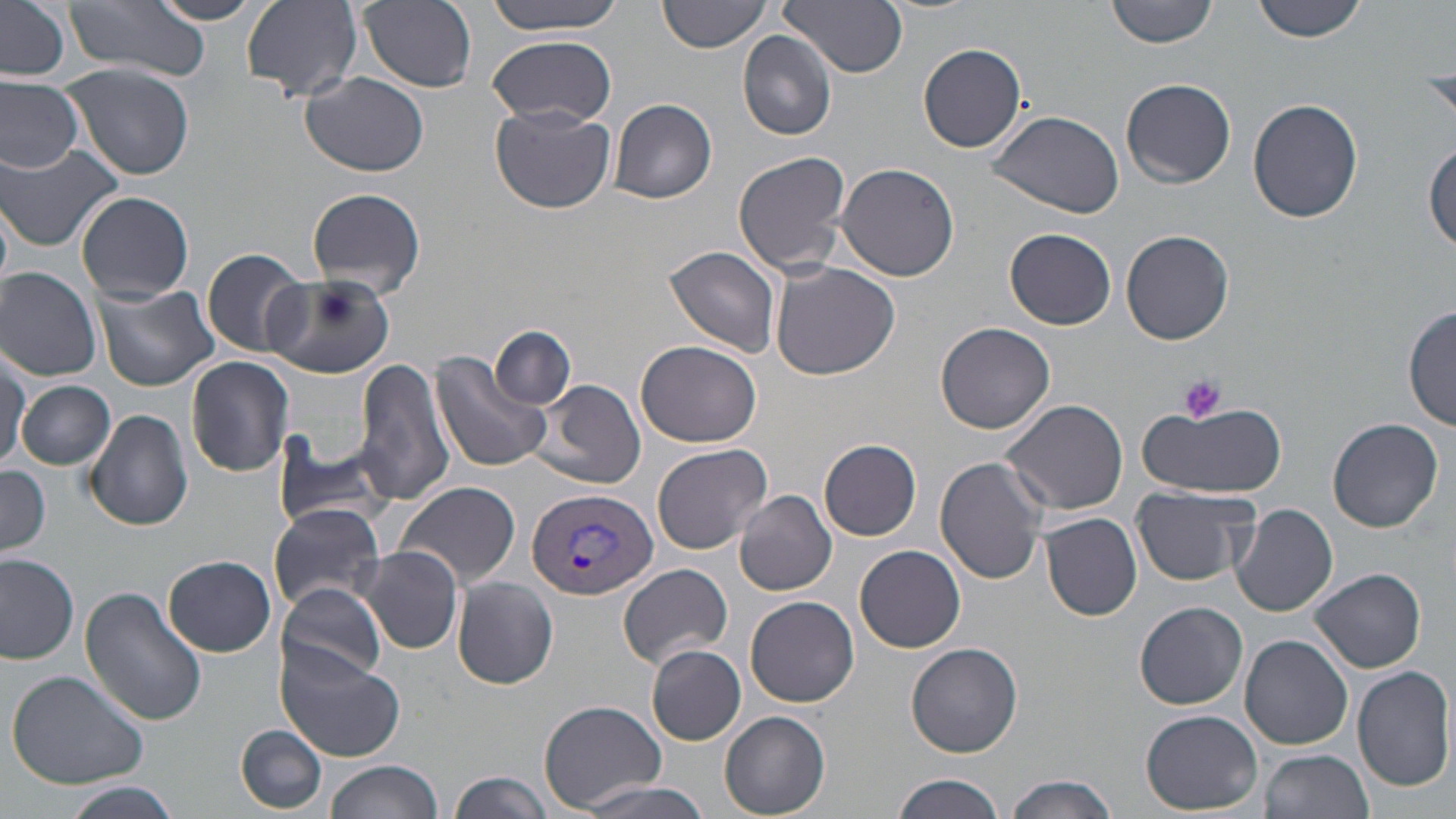

Summary:
  - Coordinate format: approximate bounding boxes as (x1,y1)-(x2,y2) corner pairs in pixels
  - Uninfected red blood cell locations: (143,0)-(267,25), (241,0)-(362,101), (358,0)-(478,91), (479,0)-(632,35), (658,0)-(768,54), (779,0)-(908,78), (1106,0)-(1219,48), (1252,0)-(1369,42), (0,2)-(73,80), (66,2)-(208,82), (738,31)-(838,141), (485,35)-(618,125), (919,42)-(1028,154), (62,64)-(196,180), (302,72)-(429,177), (0,77)-(83,174), (1122,77)-(1236,188), (1248,98)-(1363,224), (607,99)-(717,204), (490,108)-(616,214), (988,109)-(1126,219), (0,142)-(122,252), (1425,143)-(1456,256), (732,151)-(851,276), (836,162)-(960,280), (306,187)-(426,299), (77,190)-(194,304), (1005,228)-(1117,329), (1120,230)-(1234,344), (663,246)-(784,357), (200,248)-(311,357), (771,262)-(901,380), (0,266)-(102,380), (266,274)-(394,379), (93,282)-(219,392), (1405,305)-(1456,432), (936,322)-(1056,433), (491,327)-(575,408), (636,340)-(766,449), (1,345)-(30,470), (430,350)-(550,472), (352,356)-(458,507), (186,357)-(295,477), (537,378)-(647,490), (18,379)-(115,470), (998,398)-(1130,516), (1137,401)-(1286,499), (84,408)-(194,531), (953,417)-(1089,571), (1326,419)-(1445,534), (270,431)-(398,534), (820,439)-(922,540), (653,443)-(773,555), (935,456)-(1048,586), (0,465)-(51,557), (397,480)-(520,587), (1130,486)-(1261,586), (735,490)-(838,596), (269,501)-(388,611), (1231,504)-(1338,617), (1041,513)-(1143,621), (855,545)-(966,653), (356,546)-(464,654), (0,554)-(78,663), (165,555)-(275,656), (619,562)-(733,668), (1311,568)-(1426,674), (453,577)-(558,689), (275,582)-(391,684), (79,588)-(206,726), (745,596)-(859,708), (1135,601)-(1248,710), (1240,635)-(1354,750), (907,644)-(1023,759), (646,645)-(746,745), (275,647)-(404,762), (1354,666)-(1456,792), (7,668)-(151,789), (539,699)-(666,811), (1141,709)-(1261,815), (717,710)-(832,818), (238,725)-(327,814), (1258,749)-(1374,819), (325,760)-(439,819), (449,769)-(554,819), (891,773)-(1006,819), (1003,774)-(1120,818), (575,780)-(715,818), (62,783)-(183,818)
  - Plasmodium vivax-infected red blood cell locations: (527,487)-(657,601)
  - Platelet locations: (1178,374)-(1228,424)
  - Slide-level diagnosis: Plasmodium vivax
  - Field of view: one of a larger specimen
  - Image size: 1456×819 pixels
  - Magnification: 1000x
  - Stain: May-Grünwald-Giemsa
  - Preparation: thin blood film
  - Modality: light microscopy